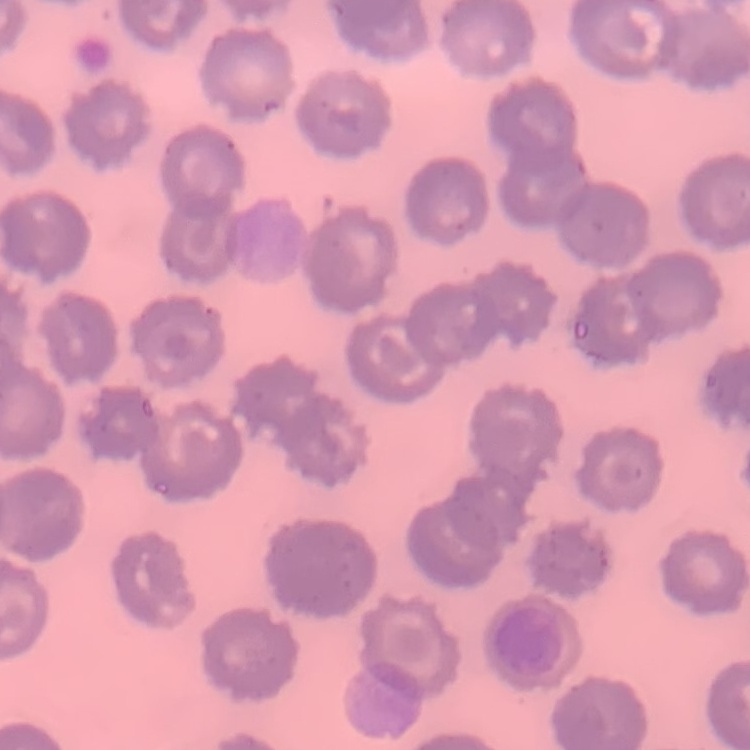
The red blood cells show no rouleaux formation. One tile cut from a larger photomicrograph. Thin blood film. Stained with either Field's or Giemsa.